Outline each blood parasite and name the species.
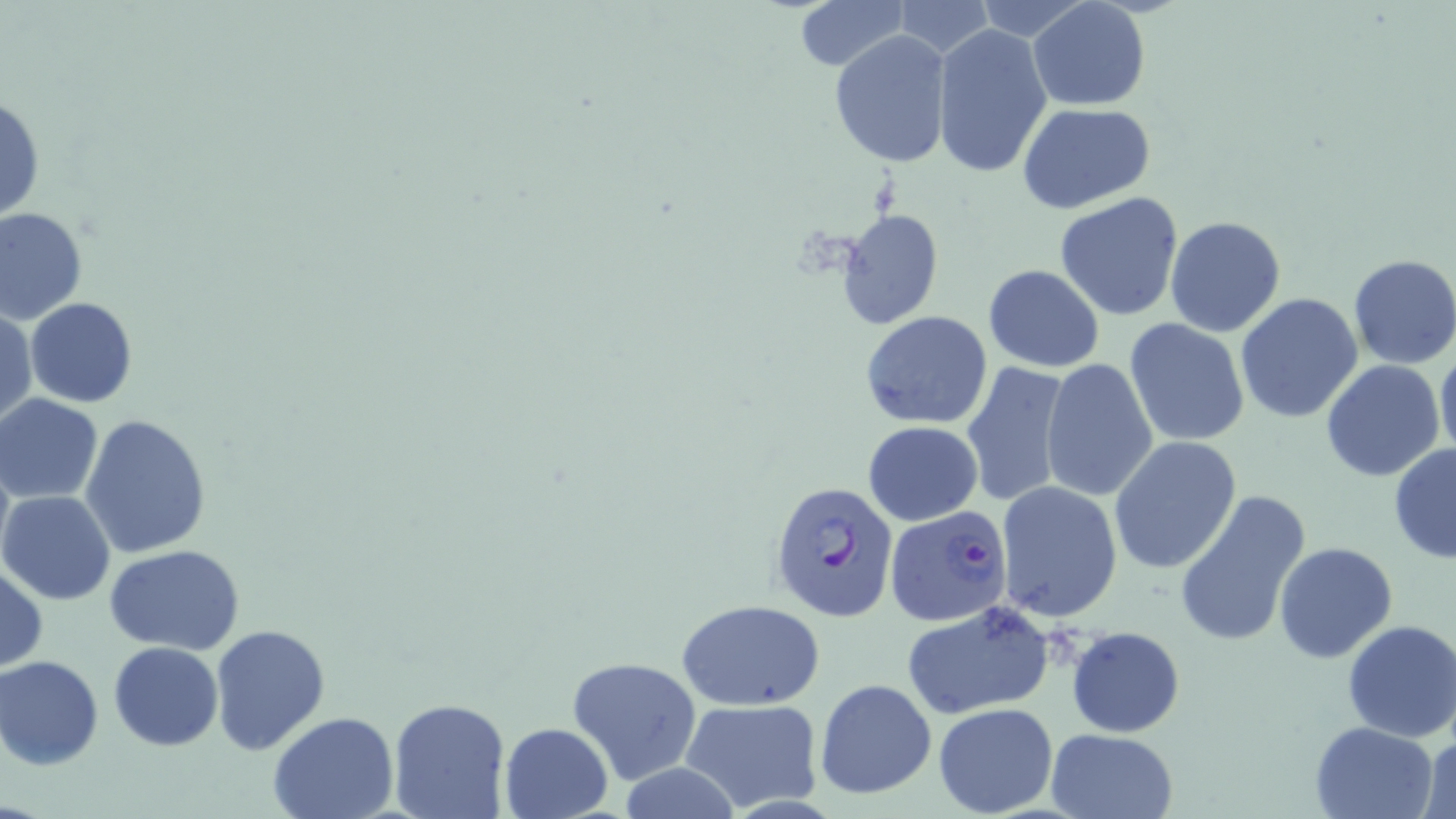

Approximate bounding boxes as named x1/y1/x2/y2 corners in pixels.
Plasmodium falciparum-infected red blood cells: (x1=768, y1=479, x2=899, y2=621), (x1=885, y1=501, x2=1015, y2=641).
No Plasmodium ovale, Plasmodium malariae, Plasmodium vivax, Babesia divergens, or Trypanosoma brucei observed.

Summary:
  - Uninfected red blood cell locations: (x1=792, y1=0, x2=909, y2=72), (x1=891, y1=1, x2=994, y2=59), (x1=1028, y1=1, x2=1149, y2=111), (x1=933, y1=24, x2=1054, y2=180), (x1=828, y1=33, x2=952, y2=168), (x1=0, y1=92, x2=46, y2=226), (x1=1016, y1=103, x2=1156, y2=214), (x1=1054, y1=191, x2=1185, y2=321), (x1=0, y1=208, x2=88, y2=324), (x1=837, y1=209, x2=945, y2=330), (x1=1164, y1=215, x2=1285, y2=337), (x1=1348, y1=254, x2=1456, y2=370), (x1=983, y1=265, x2=1104, y2=372), (x1=1235, y1=294, x2=1364, y2=424), (x1=24, y1=298, x2=137, y2=407), (x1=1, y1=306, x2=36, y2=430), (x1=860, y1=310, x2=994, y2=429), (x1=1124, y1=318, x2=1251, y2=448), (x1=1436, y1=344, x2=1456, y2=467), (x1=1041, y1=359, x2=1159, y2=505), (x1=961, y1=360, x2=1074, y2=508), (x1=1320, y1=360, x2=1446, y2=483), (x1=1, y1=394, x2=103, y2=504), (x1=80, y1=414, x2=213, y2=560), (x1=865, y1=421, x2=981, y2=525), (x1=1109, y1=437, x2=1242, y2=575), (x1=1388, y1=443, x2=1456, y2=563), (x1=995, y1=481, x2=1122, y2=622), (x1=1172, y1=487, x2=1314, y2=650), (x1=1, y1=491, x2=117, y2=605), (x1=1273, y1=542, x2=1396, y2=662), (x1=104, y1=543, x2=246, y2=655), (x1=0, y1=561, x2=47, y2=674), (x1=899, y1=600, x2=1052, y2=719), (x1=678, y1=601, x2=824, y2=711), (x1=1342, y1=619, x2=1456, y2=742), (x1=209, y1=624, x2=330, y2=756), (x1=1065, y1=626, x2=1184, y2=737), (x1=108, y1=641, x2=225, y2=750), (x1=0, y1=655, x2=105, y2=770), (x1=568, y1=655, x2=700, y2=784), (x1=813, y1=678, x2=937, y2=800), (x1=387, y1=697, x2=511, y2=819), (x1=680, y1=699, x2=824, y2=811), (x1=933, y1=702, x2=1057, y2=817), (x1=268, y1=712, x2=399, y2=819), (x1=1309, y1=720, x2=1438, y2=818), (x1=498, y1=721, x2=616, y2=818), (x1=1046, y1=728, x2=1176, y2=818), (x1=1416, y1=734, x2=1455, y2=818)
  - Slide-level diagnosis: Plasmodium falciparum
  - Modality: light microscopy
  - Field of view: one of a larger specimen
  - Image size: 1456×819 pixels
  - Stain: May-Grünwald-Giemsa
  - Preparation: thin blood film
  - Magnification: 1000x